Assess for malaria.
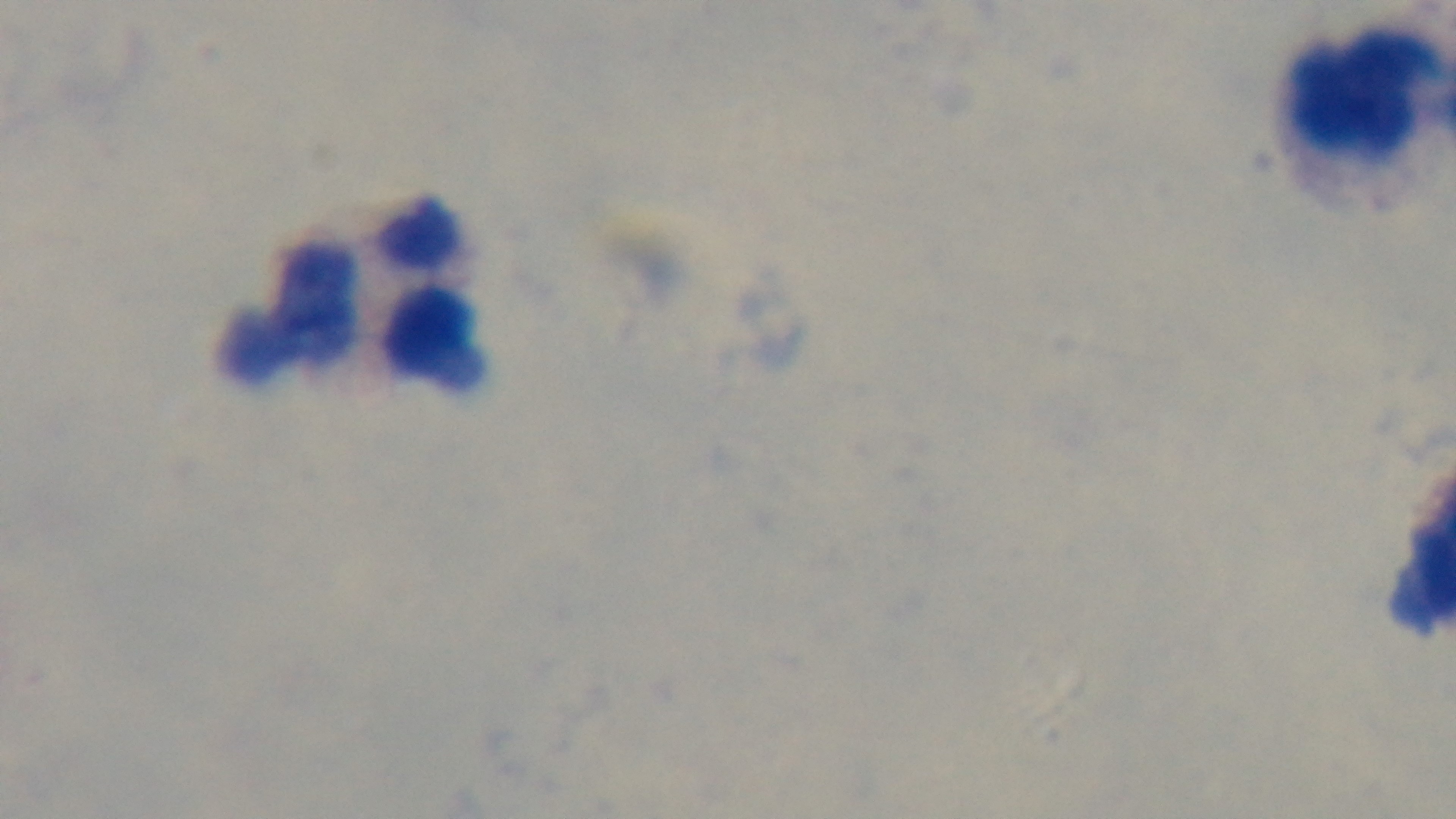

Uninfected.

100x oil-immersion objective. Giemsa-stained. Light microscopy. Mounted 4K digital camera. Preparation: thick smear. Single field of view.